Report the malaria status of this cell.
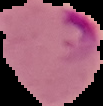
It is parasitized.

Segmented cell region on a black background. From a thin blood film. Image is 103×106 pixels.